Give the extent of all uninfected red blood cells.
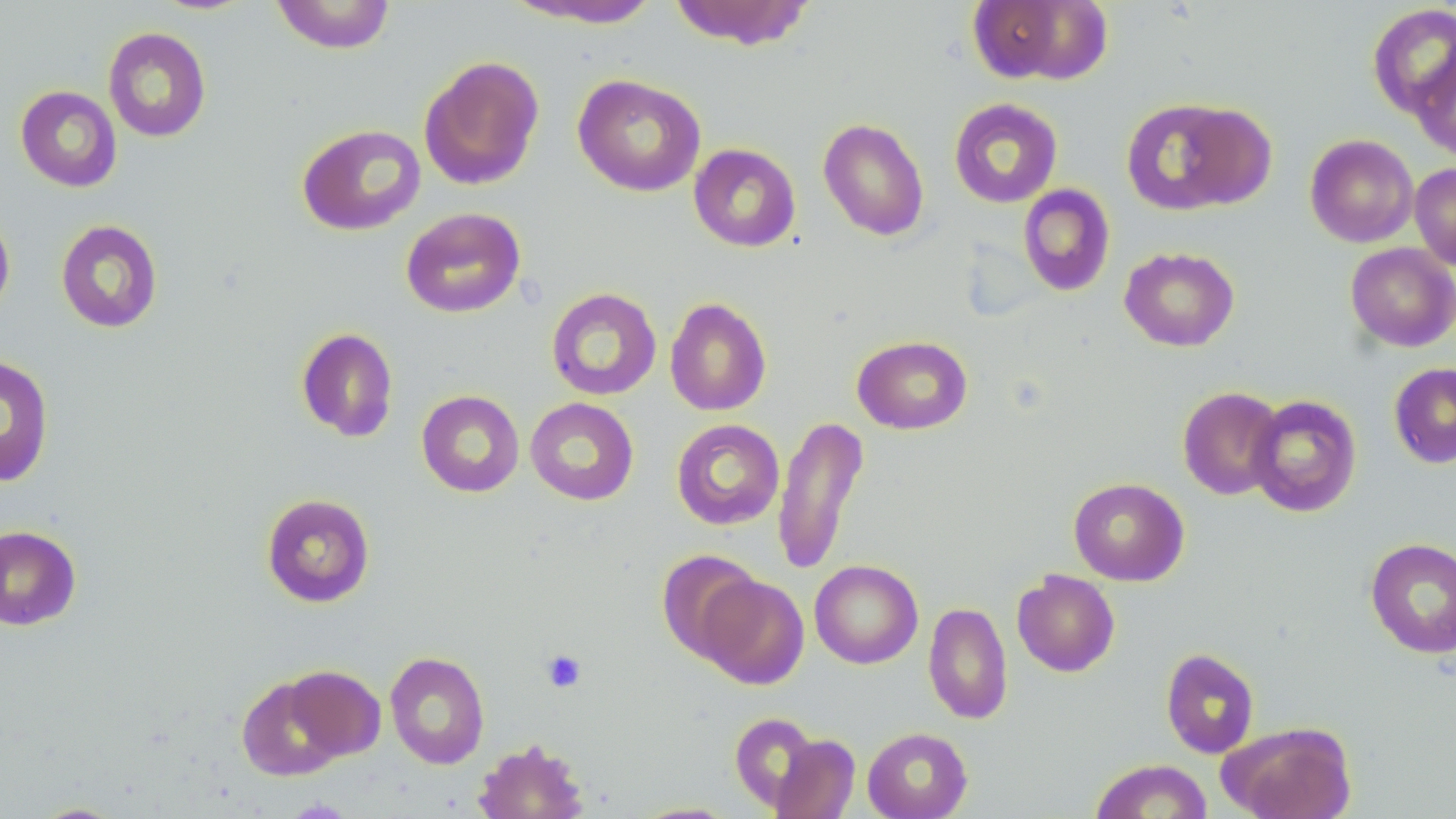
Approximate bounding boxes as (x1, y1, x2, y2) in pixels.
Uninfected red blood cells: (270, 0, 396, 54), (503, 0, 663, 29), (668, 0, 815, 50), (966, 0, 1113, 86), (1367, 3, 1456, 120), (102, 26, 212, 143), (1411, 50, 1456, 161), (418, 55, 545, 191), (572, 73, 706, 197), (15, 85, 122, 192), (1120, 97, 1262, 215), (948, 98, 1063, 208), (817, 117, 930, 241), (296, 123, 426, 236), (1305, 134, 1418, 247), (688, 143, 801, 252), (1409, 163, 1456, 271), (1017, 184, 1115, 297), (0, 207, 15, 319), (400, 207, 526, 318), (56, 219, 163, 334), (1345, 242, 1456, 352), (1119, 246, 1240, 352), (546, 287, 662, 401), (665, 296, 772, 416), (295, 327, 399, 443), (852, 334, 973, 435), (0, 354, 55, 488), (1388, 362, 1456, 469), (1177, 386, 1286, 500), (416, 390, 524, 497), (1247, 395, 1362, 517), (525, 397, 639, 506), (772, 415, 869, 575), (671, 419, 785, 530), (1068, 477, 1190, 586), (260, 493, 376, 607), (0, 525, 82, 631), (1365, 537, 1456, 659), (656, 549, 764, 663), (809, 559, 923, 669), (1012, 569, 1121, 677), (697, 573, 809, 689), (923, 601, 1013, 725), (1161, 648, 1260, 759), (385, 651, 490, 769), (283, 665, 386, 761), (236, 674, 348, 781), (729, 711, 821, 813), (1219, 722, 1357, 819), (862, 727, 973, 819), (770, 734, 860, 818), (473, 738, 590, 819), (1089, 759, 1213, 818), (628, 801, 742, 818), (29, 802, 130, 818).

Platelet locations: (540, 649, 587, 693). Slide-level diagnosis: negative for blood parasites. One field of a larger specimen. Light microscopy. May-Grünwald-Giemsa-stained preparation. Captured at 1000x magnification. Thin blood smear. Image is 1456×819 pixels.